Describe the morphology of the red blood cells.
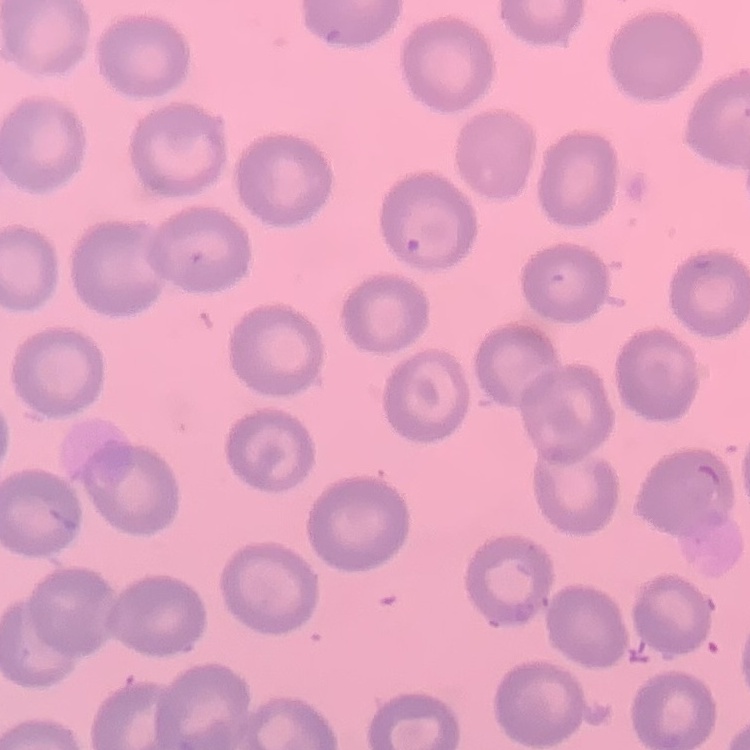

They show no rouleaux formation.

image type = one tile cut from a larger photomicrograph
preparation = thin peripheral smear
stain = Field's or Giemsa